Evaluate for malaria.
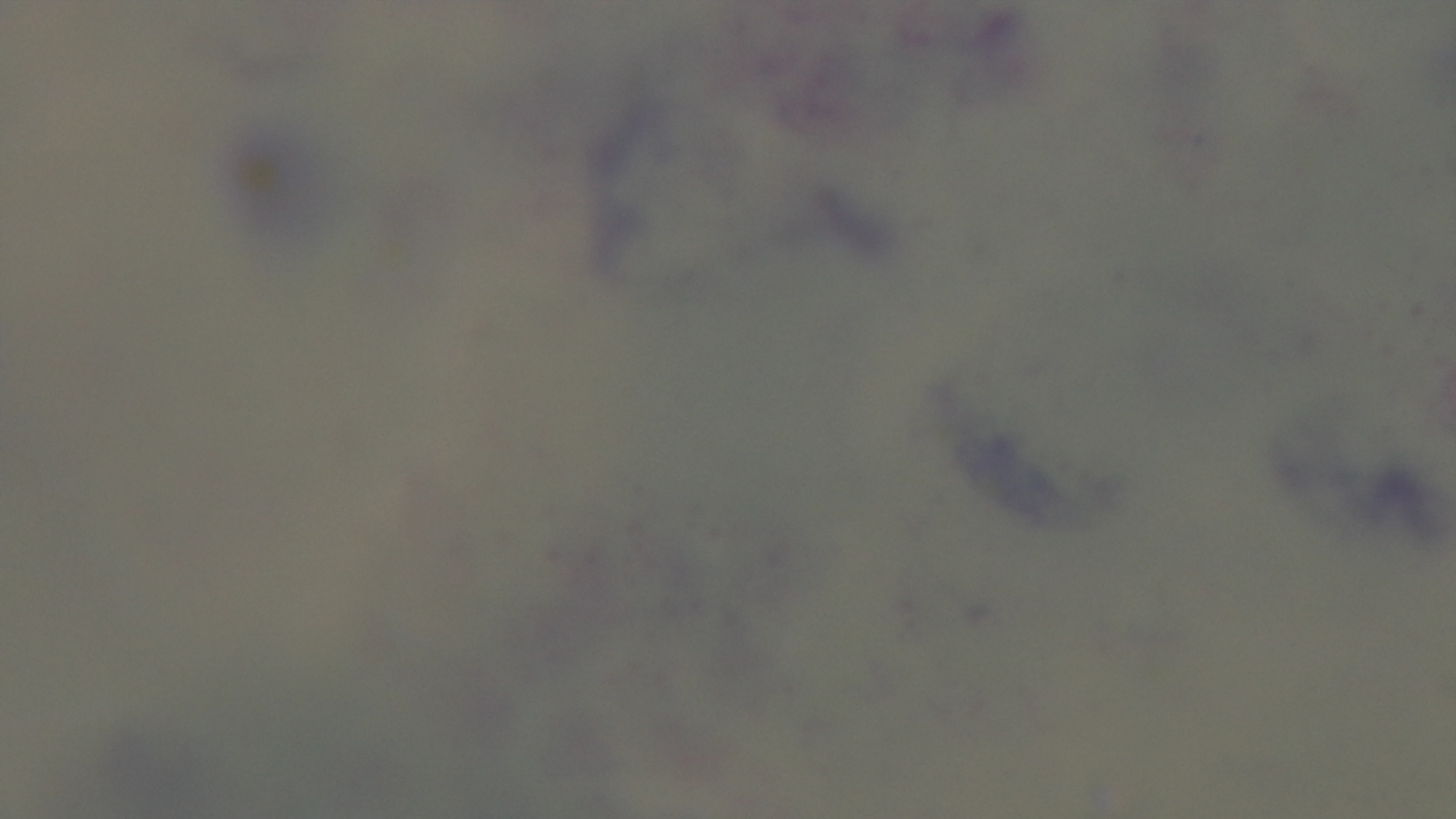

Negative.

capture = mounted 4K digital camera
objective = 100x oil immersion
field of view = single
modality = light microscopy
preparation = thick
stain = Giemsa